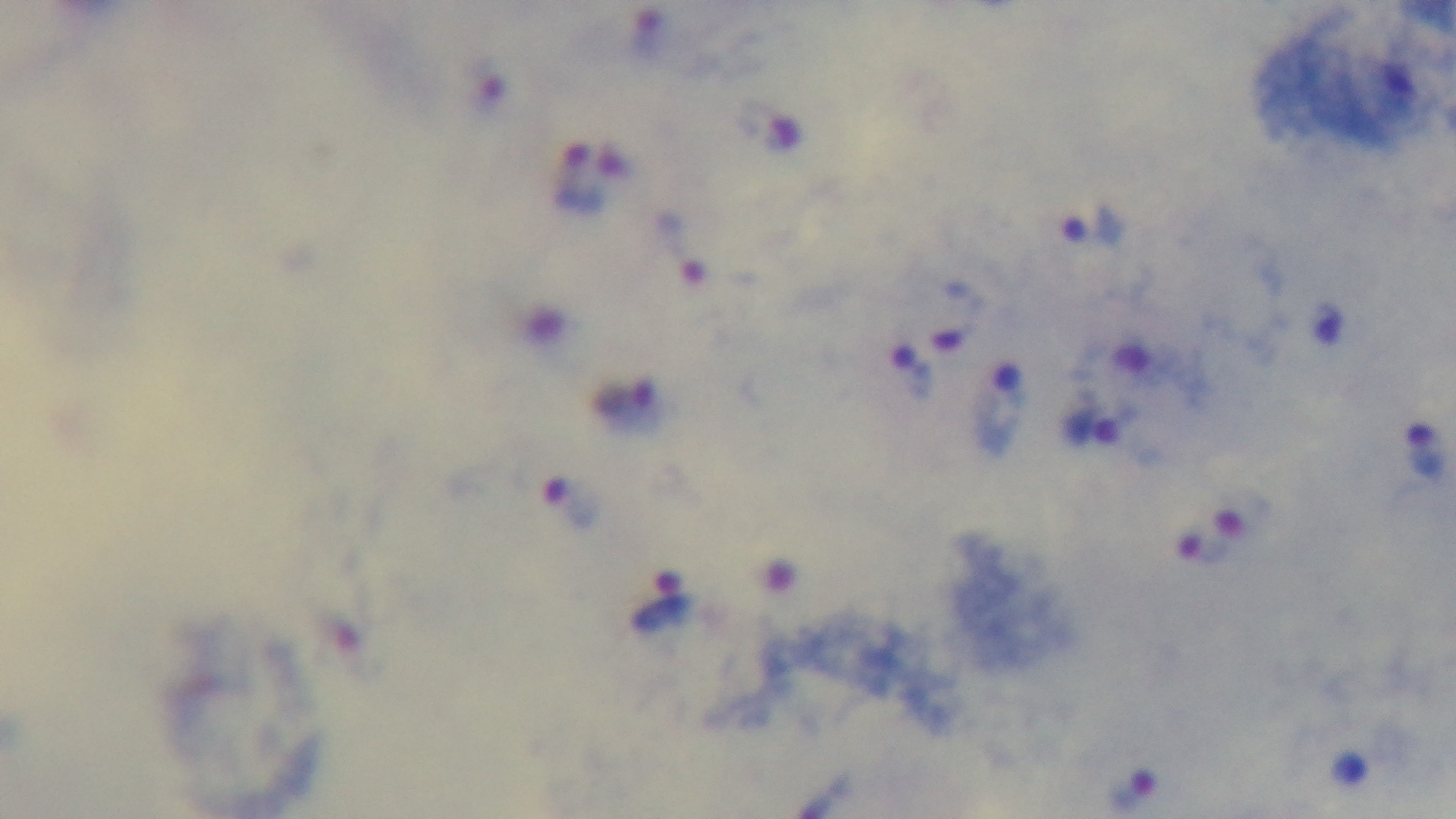

objective: 100x oil immersion
malaria_status: positive
stain: Giemsa
modality: light microscopy
field_of_view: single
capture: mounted 4K digital camera
preparation: thick